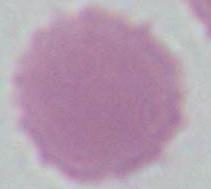
identification = erythrocyte
modality = photomicrograph
magnification = 1000x